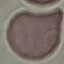

Summary:
  - Malaria status: uninfected
  - Image type: automatically extracted cell patch, resized to 64 × 64 pixels
  - Capture: smartphone camera at the microscope eyepiece
  - Preparation: thin smear
  - Stain: Giemsa